Locate platelets.
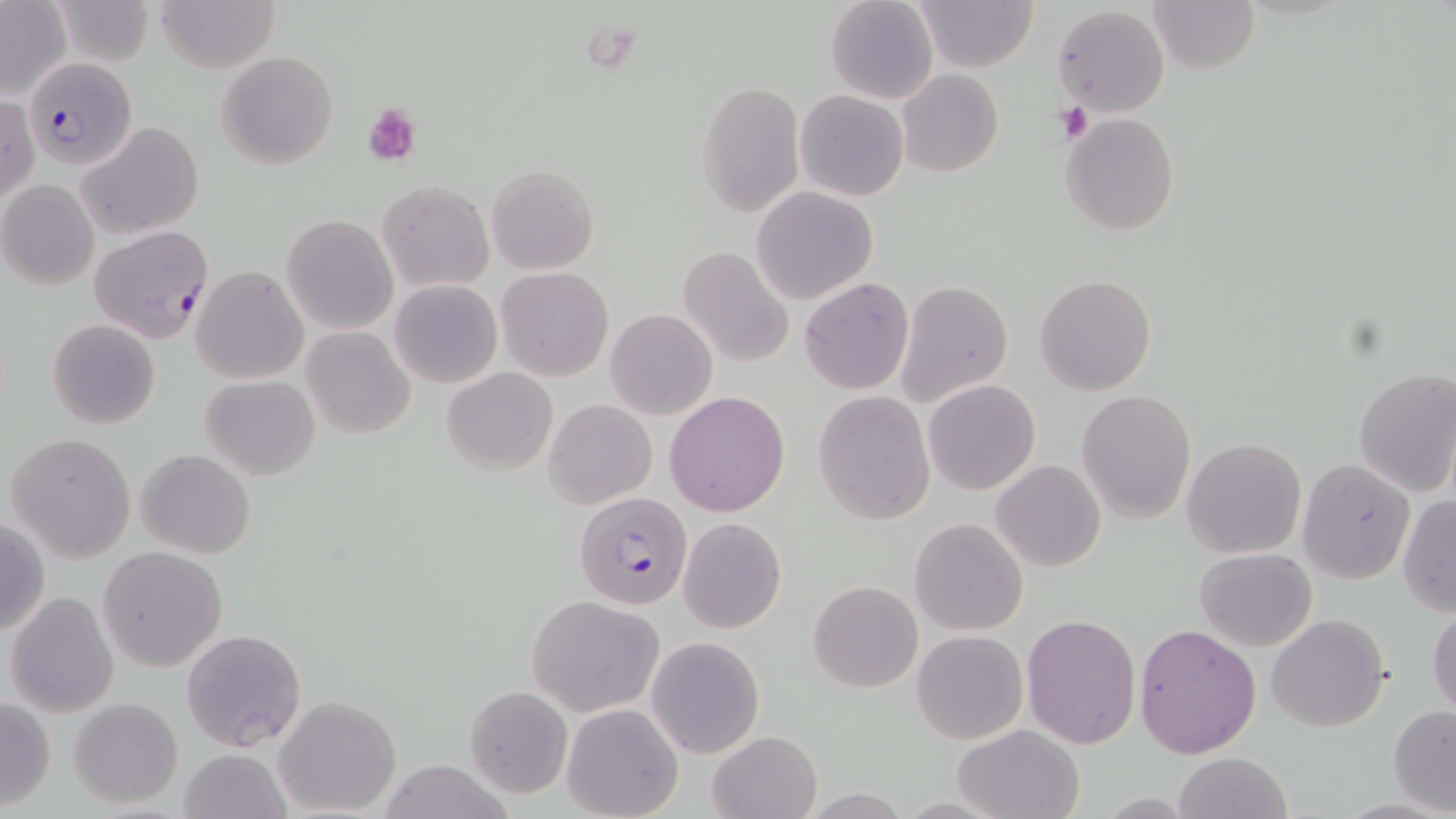

Approximate bounding boxes as (x1,y1)-(x2,y2) corner pairs in pixels.
Platelets: (1054,99)-(1094,144), (363,101)-(421,164).

Uninfected red blood cell locations: (53,0)-(153,69), (154,0)-(280,72), (825,0)-(939,105), (1148,0)-(1260,73), (917,1)-(1036,72), (0,3)-(71,100), (1053,5)-(1169,117), (217,51)-(338,170), (898,69)-(1003,178), (697,79)-(805,217), (795,90)-(908,202), (1,95)-(38,207), (1061,113)-(1180,237), (75,122)-(205,240), (486,164)-(598,275), (0,180)-(100,290), (378,180)-(494,294), (750,186)-(877,305), (281,214)-(396,334), (678,247)-(794,368), (192,266)-(308,384), (496,267)-(613,381), (1034,273)-(1156,396), (799,277)-(914,395), (390,279)-(502,388), (897,280)-(1013,406), (605,308)-(718,420), (48,319)-(161,429), (301,326)-(415,438), (442,367)-(557,475), (1353,367)-(1456,496), (201,374)-(320,480), (923,379)-(1040,495), (1076,389)-(1196,522), (813,390)-(934,524), (664,391)-(790,517), (543,398)-(657,510), (6,432)-(137,561), (1182,438)-(1306,557), (135,448)-(256,559), (1297,458)-(1417,585), (991,459)-(1106,572), (1397,495)-(1456,617), (678,517)-(786,634), (0,518)-(49,638), (909,518)-(1028,636), (98,546)-(228,672), (1195,547)-(1318,651), (808,580)-(922,691), (6,592)-(120,717), (527,594)-(664,717), (1428,607)-(1456,718), (1021,613)-(1142,749), (1267,613)-(1391,733), (1133,623)-(1262,760), (180,628)-(307,751), (912,629)-(1027,745), (646,637)-(764,758), (465,686)-(573,798), (273,695)-(401,816), (0,696)-(56,811), (69,697)-(184,808), (561,703)-(683,819), (1389,705)-(1456,814), (954,723)-(1084,819), (708,731)-(823,819), (179,749)-(291,819), (1173,752)-(1293,819), (377,759)-(517,819). Plasmodium falciparum-infected red blood cell locations: (24,58)-(137,169), (87,225)-(214,344), (573,490)-(693,610). Slide-level diagnosis: Plasmodium falciparum. Optical microscopy. Image is 1456×819 pixels. May-Grünwald-Giemsa stain. One field of a larger specimen. Thin blood smear. Captured at 1000x magnification.